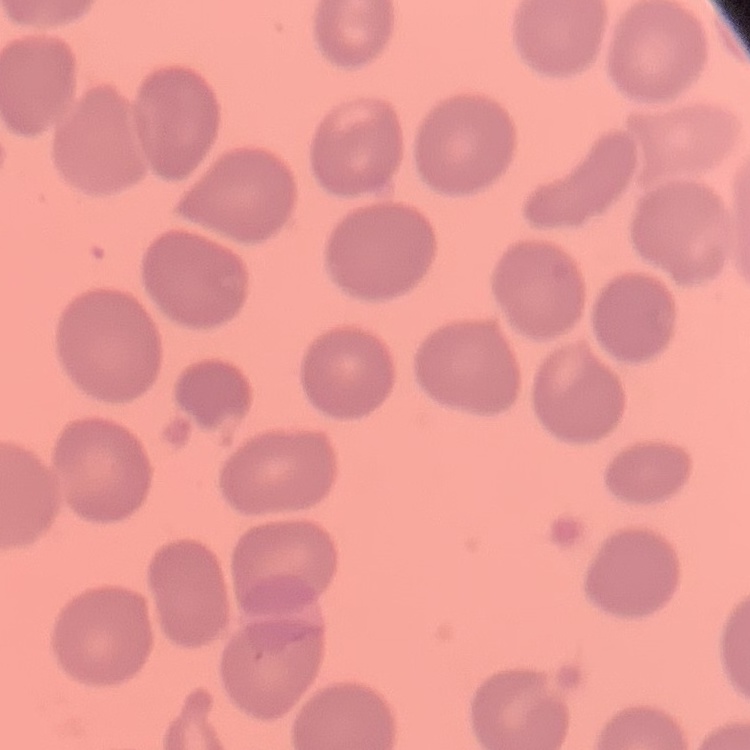

Summary:
  - Red blood cell morphology: no rouleaux formation
  - Stain: Field's or Giemsa
  - Image type: one tile cut from a larger photomicrograph
  - Preparation: thin blood film